Classify this cell by malaria status.
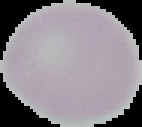

It is uninfected.

{
  "image_size": "142×127 pixels",
  "image_type": "cell region segmented out of the field of view; surrounding area masked to black",
  "preparation": "thin blood film"
}